Assess the morphology of the erythrocytes.
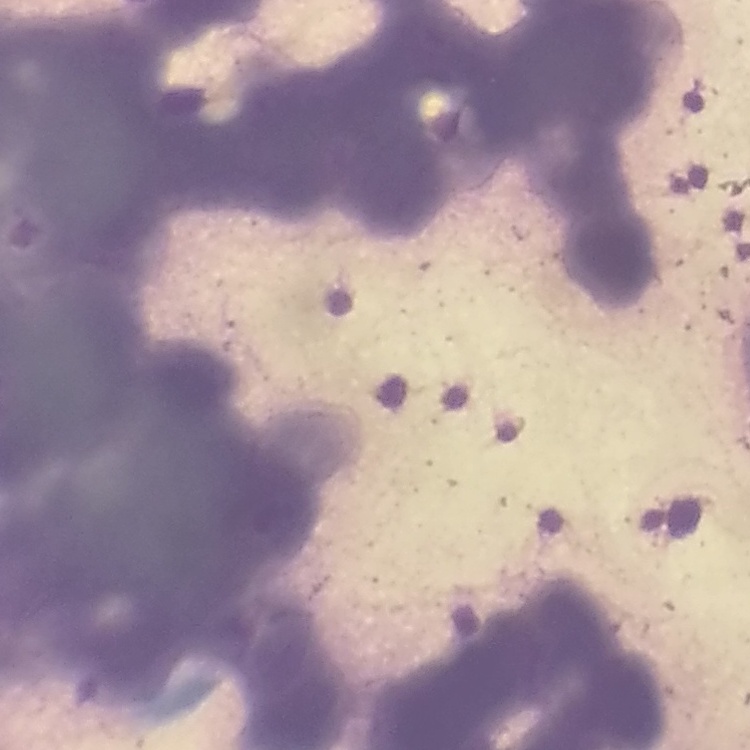
They show rouleaux formation.

Summary:
  - Stain: Field's or Giemsa
  - Preparation: thin blood film
  - Image type: square crop of a larger photomicrograph